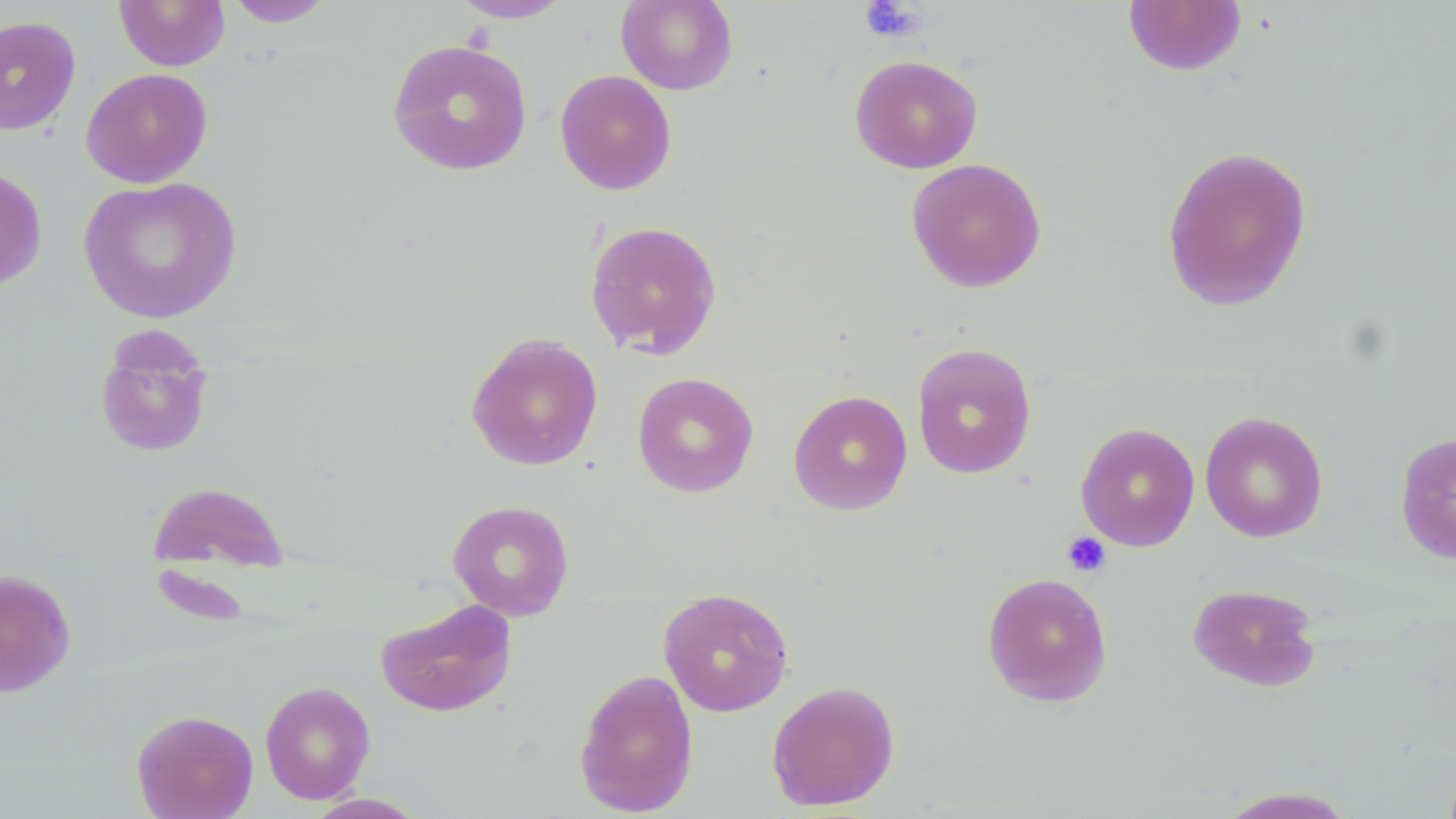
Summary:
  - Coordinate format: approximate bounding boxes as (x1,y1)-(x2,y2) corner pairs in pixels
  - Platelet locations: (858,1)-(927,44), (1062,531)-(1110,578)
  - Uninfected red blood cell locations: (115,0)-(230,71), (224,0)-(335,27), (448,0)-(574,23), (616,0)-(738,95), (1122,1)-(1247,76), (0,14)-(81,135), (386,38)-(532,176), (849,54)-(983,174), (80,68)-(213,188), (555,69)-(677,195), (1160,144)-(1313,312), (907,157)-(1047,292), (0,166)-(48,292), (78,176)-(242,324), (584,219)-(723,359), (94,327)-(216,458), (465,332)-(604,471), (912,343)-(1037,478), (632,371)-(759,498), (788,389)-(913,515), (1200,411)-(1328,543), (1075,422)-(1200,551), (1394,431)-(1456,565), (146,480)-(291,576), (447,500)-(575,620), (0,569)-(76,697), (981,572)-(1113,707), (1187,582)-(1322,692), (658,586)-(794,716), (375,598)-(517,717), (574,668)-(699,816), (259,680)-(376,805), (766,680)-(900,811), (131,709)-(259,819), (1213,786)-(1359,818)
  - Slide-level diagnosis: negative for blood parasites
  - Modality: optical microscopy
  - Stain: May-Grünwald-Giemsa
  - Image size: 1456×819 pixels
  - Preparation: thin blood film
  - Field of view: one of a larger specimen
  - Magnification: 1000x